Give the position of every leukocyte visible.
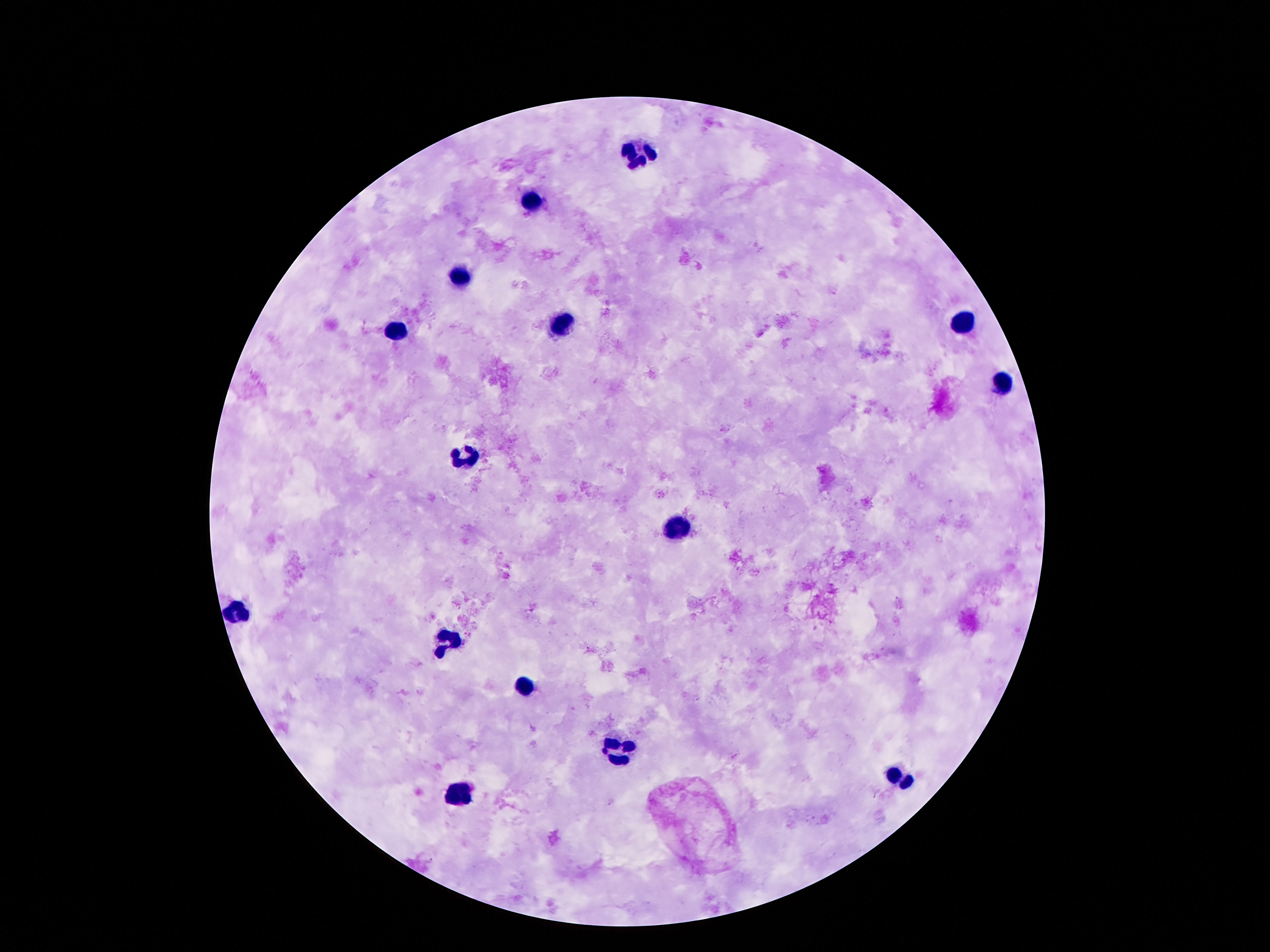
Approximate centers as [x, y] in pixels.
Leukocytes: [636, 152], [533, 199], [461, 273], [961, 325], [564, 327], [396, 332], [1002, 386], [466, 457], [678, 532], [240, 608], [449, 640], [526, 684], [618, 750], [898, 780], [459, 794].

Giemsa stain. 100x magnification. One field from this slide. Patient malaria status: negative. Thick blood film. Image is 1270×952 pixels. Smartphone photograph taken through the microscope eyepiece.